Look for Plasmodium parasites.
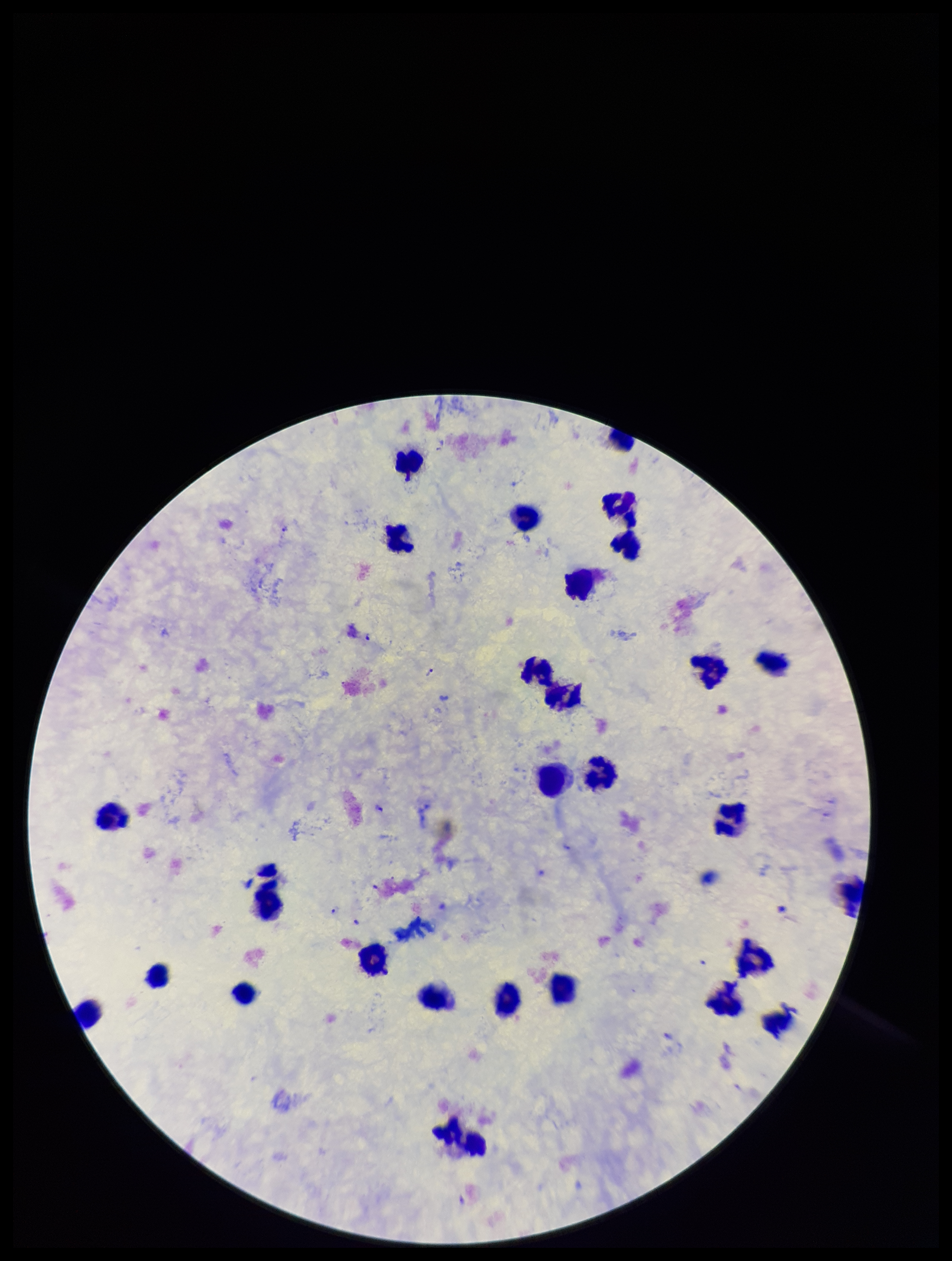
Seen.

capture = smartphone photograph through the microscope eyepiece
preparation = thick smear
leukocyte count = 29
image size = 952×1261 pixels
parasite count = 7
species reported for this patient = Plasmodium falciparum
field of view = single
stain = Giemsa
patient malaria status = infected